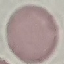
Summary:
  - Malaria status: uninfected
  - Stain: Giemsa
  - Preparation: thin blood film
  - Capture: smartphone camera at the microscope eyepiece
  - Image type: cell patch, automatically extracted from a larger field of view and resized to 64 × 64 pixels